Classify this cell by malaria status.
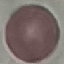
Uninfected.

Summary:
  - Image type: automatically extracted cell patch, resized to 64 × 64 pixels
  - Stain: Giemsa
  - Capture: smartphone through the microscope eyepiece
  - Preparation: thin blood smear